Comment on the morphology of the erythrocytes.
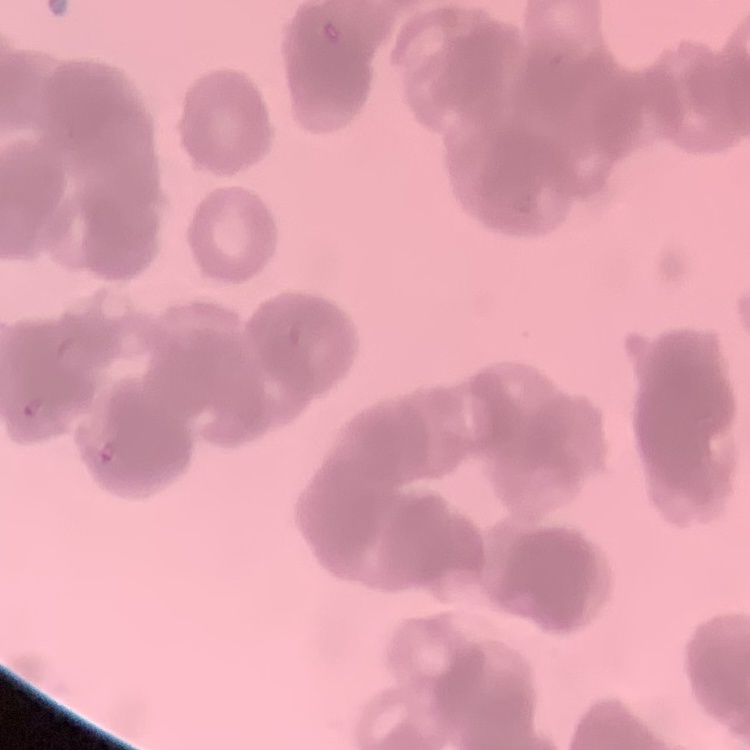
Rouleaux formation.

Summary:
  - Stain: Field's or Giemsa
  - Preparation: thin blood film
  - Image type: square crop of a larger photomicrograph